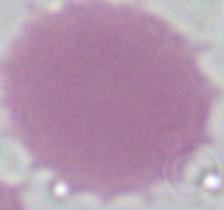

Micrograph. Captured at 1000x magnification. An erythrocyte is shown.